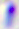
Captured at 400x magnification. Toxoplasma gondii is seen. Photomicrograph.